Give the extent of all Plasmodium ovale-infected red blood cells.
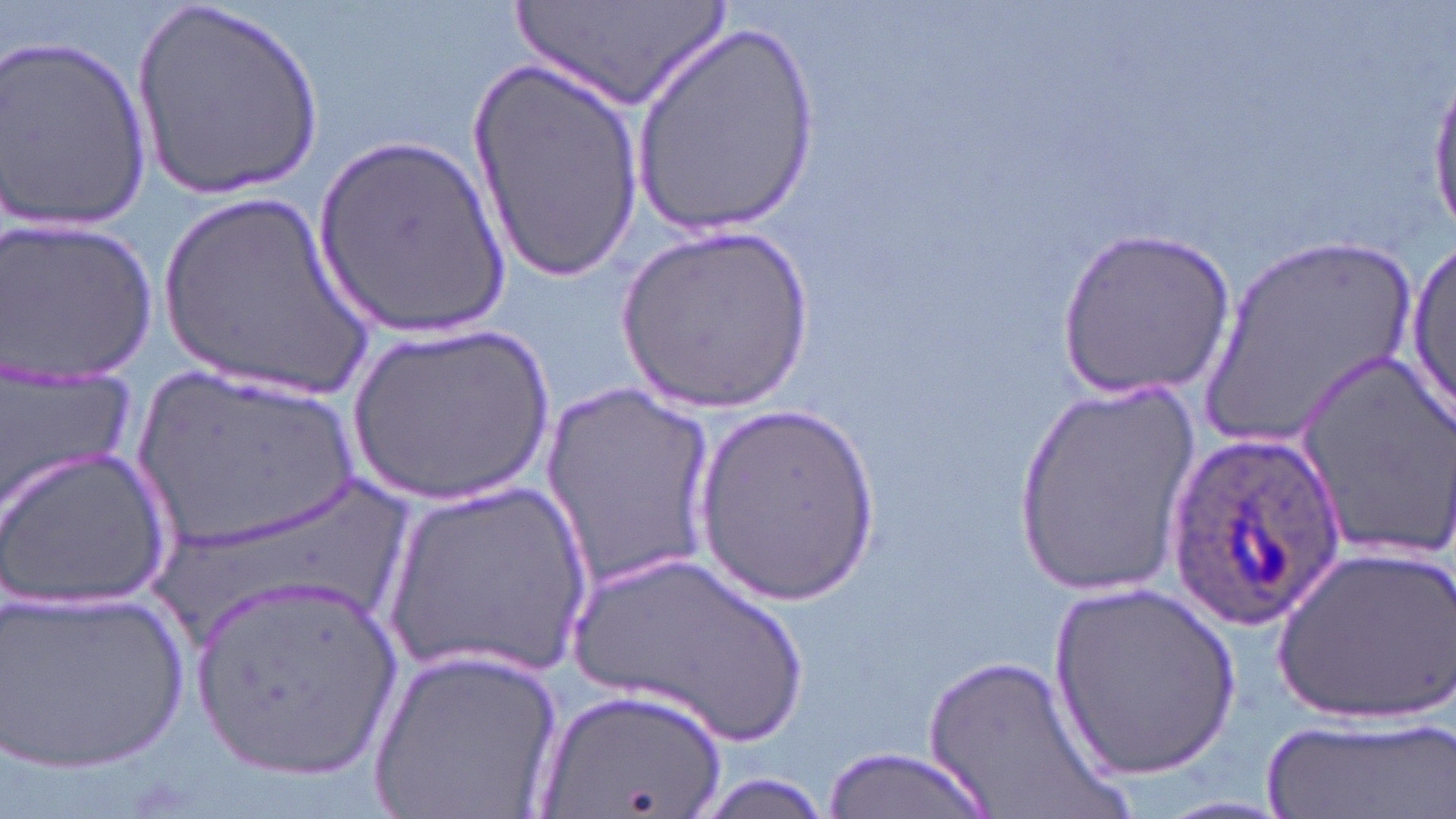
Approximate bounding boxes as named x1/y1/x2/y2 corners in pixels.
Plasmodium ovale-infected red blood cells: (x1=1161, y1=427, x2=1346, y2=634).

Uninfected red blood cell locations: (x1=135, y1=0, x2=326, y2=201), (x1=508, y1=0, x2=737, y2=107), (x1=630, y1=21, x2=820, y2=236), (x1=2, y1=34, x2=155, y2=234), (x1=469, y1=55, x2=644, y2=283), (x1=1428, y1=79, x2=1456, y2=236), (x1=313, y1=134, x2=515, y2=342), (x1=151, y1=182, x2=382, y2=400), (x1=2, y1=214, x2=159, y2=382), (x1=617, y1=224, x2=813, y2=416), (x1=1057, y1=229, x2=1234, y2=401), (x1=1187, y1=235, x2=1429, y2=457), (x1=1406, y1=243, x2=1455, y2=422), (x1=346, y1=320, x2=554, y2=505), (x1=1295, y1=347, x2=1456, y2=557), (x1=126, y1=361, x2=368, y2=552), (x1=0, y1=373, x2=139, y2=519), (x1=1011, y1=379, x2=1202, y2=598), (x1=540, y1=380, x2=717, y2=590), (x1=698, y1=406, x2=881, y2=613), (x1=0, y1=445, x2=170, y2=612), (x1=144, y1=466, x2=417, y2=662), (x1=380, y1=477, x2=597, y2=686), (x1=1270, y1=544, x2=1453, y2=724), (x1=562, y1=547, x2=817, y2=749), (x1=191, y1=576, x2=407, y2=780), (x1=1050, y1=582, x2=1240, y2=784), (x1=1, y1=583, x2=191, y2=777), (x1=369, y1=642, x2=564, y2=819), (x1=915, y1=654, x2=1126, y2=819), (x1=535, y1=685, x2=734, y2=819), (x1=1262, y1=710, x2=1451, y2=819), (x1=822, y1=747, x2=998, y2=819), (x1=685, y1=773, x2=840, y2=818). Slide-level diagnosis: Plasmodium ovale. Optical microscopy. May-Grünwald-Giemsa stain. One field of a larger specimen. Image is 1456×819 pixels. 1000x magnification. Thin blood smear.